Classify this cell by malaria status.
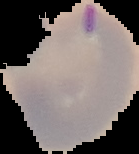

Parasitized.

image size = 139×154 pixels
preparation = thin blood film
image type = segmented cell region on a black background